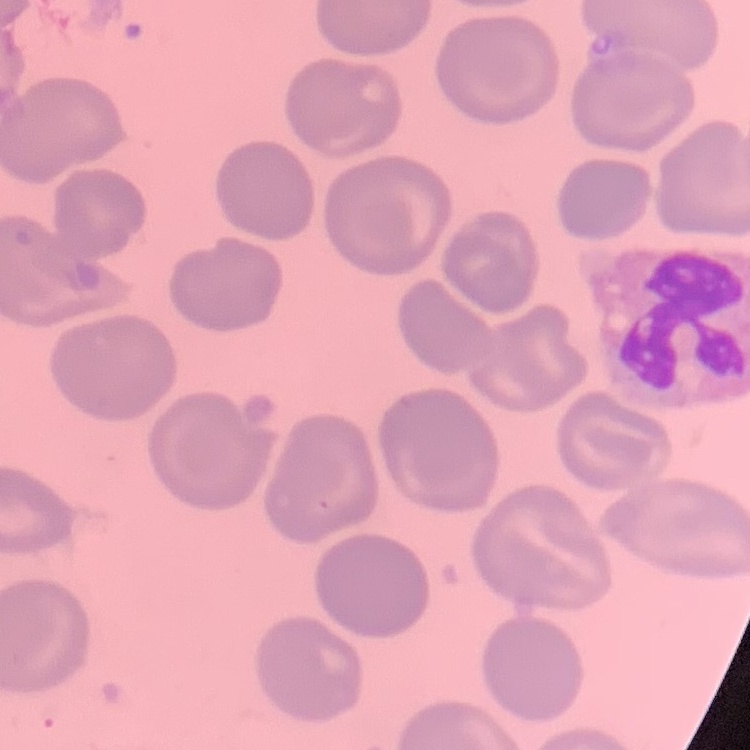 The erythrocytes show no rouleaux formation. Stained with either Field's or Giemsa. One tile cut from a larger photomicrograph. Thin peripheral smear.